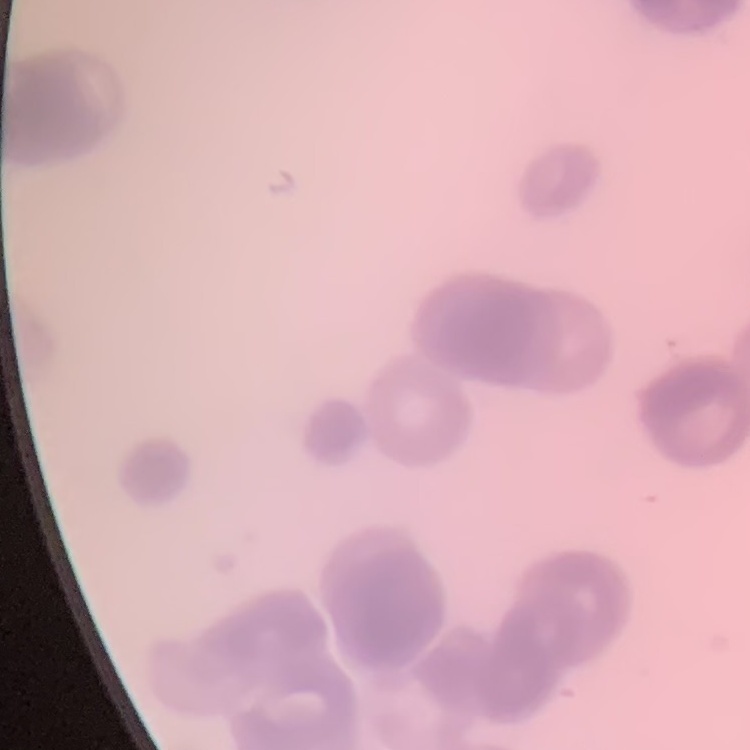
Summary:
  - Red blood cell morphology: rouleaux formation
  - Image type: square crop of a larger photomicrograph
  - Stain: Field's or Giemsa
  - Preparation: thin peripheral smear